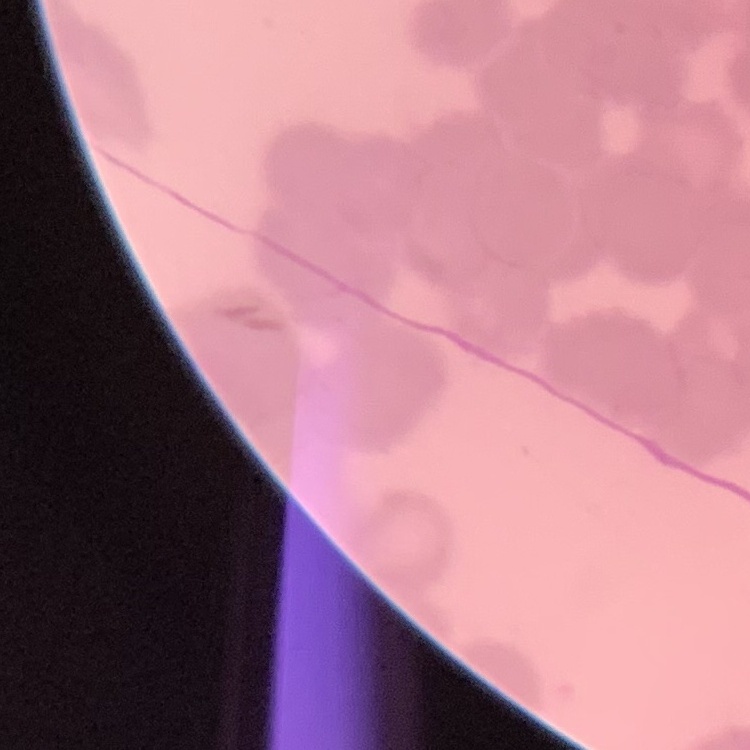
Summary:
  - Red blood cell morphology: rouleaux formation
  - Preparation: thin blood film
  - Stain: Field's or Giemsa
  - Image type: square crop of a larger photomicrograph